Outline each uninfected red blood cell.
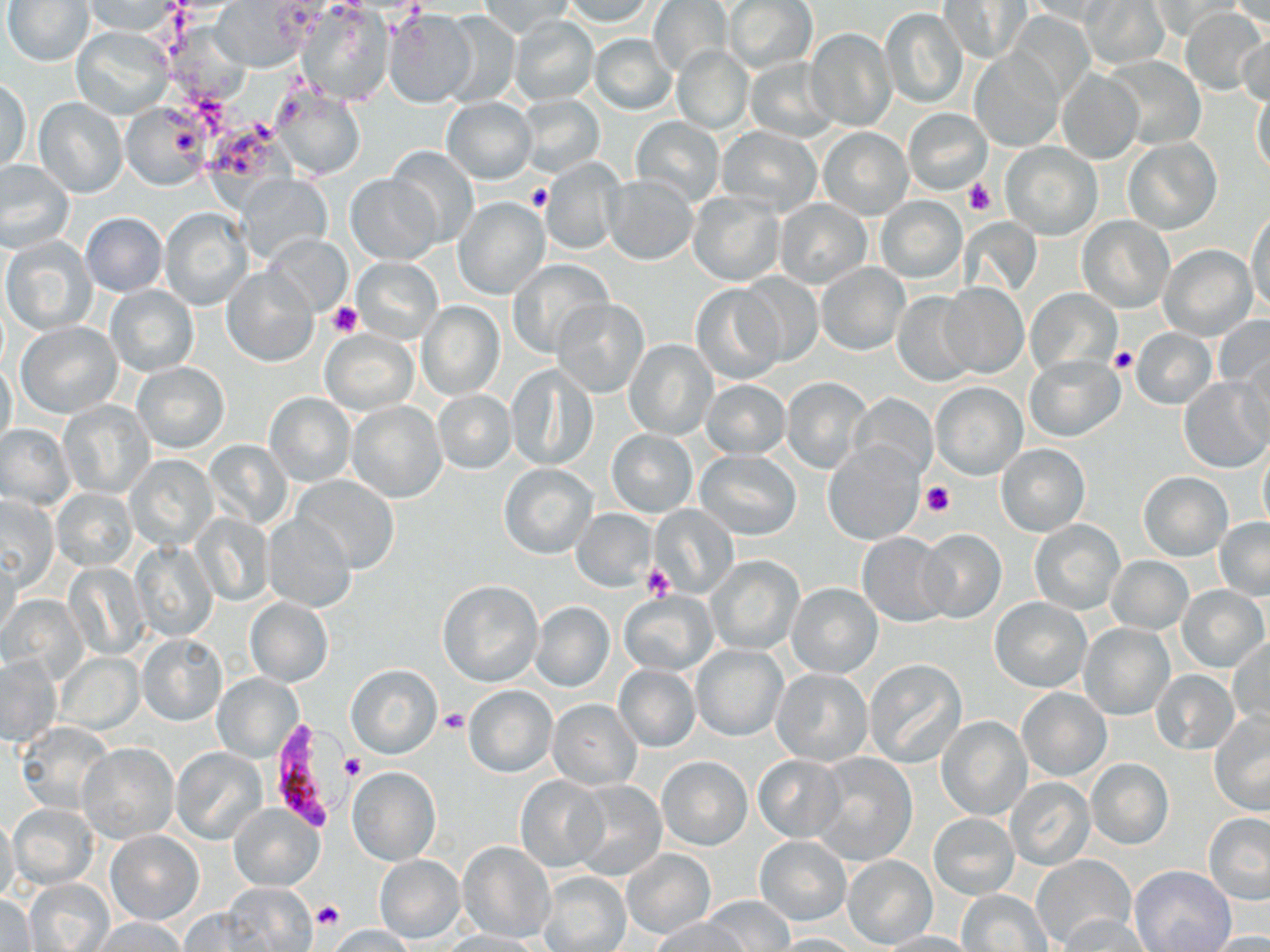

Approximate bounding boxes as named x1/y1/x2/y2 corners in pixels.
Uninfected red blood cells: (x1=4, y1=0, x2=94, y2=65), (x1=214, y1=0, x2=321, y2=70), (x1=559, y1=0, x2=662, y2=27), (x1=648, y1=0, x2=732, y2=76), (x1=725, y1=0, x2=816, y2=72), (x1=938, y1=0, x2=1029, y2=63), (x1=1084, y1=0, x2=1167, y2=68), (x1=1229, y1=0, x2=1269, y2=33), (x1=81, y1=1, x2=184, y2=38), (x1=477, y1=1, x2=575, y2=38), (x1=1020, y1=1, x2=1122, y2=25), (x1=1149, y1=1, x2=1242, y2=39), (x1=294, y1=5, x2=394, y2=106), (x1=880, y1=7, x2=970, y2=110), (x1=1182, y1=7, x2=1268, y2=96), (x1=382, y1=8, x2=478, y2=108), (x1=440, y1=12, x2=522, y2=107), (x1=507, y1=17, x2=599, y2=106), (x1=806, y1=26, x2=897, y2=133), (x1=71, y1=27, x2=173, y2=119), (x1=588, y1=33, x2=678, y2=116), (x1=1236, y1=35, x2=1269, y2=109), (x1=672, y1=45, x2=755, y2=135), (x1=969, y1=50, x2=1064, y2=152), (x1=1106, y1=55, x2=1206, y2=149), (x1=744, y1=57, x2=838, y2=142), (x1=1057, y1=68, x2=1142, y2=164), (x1=1, y1=77, x2=32, y2=171), (x1=1250, y1=84, x2=1269, y2=180), (x1=273, y1=86, x2=366, y2=182), (x1=515, y1=94, x2=605, y2=179), (x1=34, y1=97, x2=128, y2=198), (x1=441, y1=97, x2=536, y2=184), (x1=121, y1=105, x2=207, y2=189), (x1=904, y1=108, x2=991, y2=194), (x1=631, y1=117, x2=724, y2=206), (x1=716, y1=127, x2=823, y2=217), (x1=817, y1=127, x2=913, y2=219), (x1=1121, y1=137, x2=1221, y2=235), (x1=1001, y1=142, x2=1102, y2=240), (x1=385, y1=146, x2=481, y2=247), (x1=541, y1=156, x2=624, y2=257), (x1=0, y1=161, x2=75, y2=252), (x1=234, y1=173, x2=333, y2=266), (x1=345, y1=174, x2=440, y2=265), (x1=603, y1=175, x2=698, y2=265), (x1=687, y1=190, x2=785, y2=286), (x1=454, y1=195, x2=549, y2=300), (x1=875, y1=196, x2=966, y2=283), (x1=773, y1=197, x2=873, y2=289), (x1=160, y1=208, x2=253, y2=311), (x1=1247, y1=208, x2=1269, y2=316), (x1=79, y1=212, x2=168, y2=297), (x1=1076, y1=215, x2=1175, y2=313), (x1=263, y1=236, x2=351, y2=317), (x1=2, y1=237, x2=97, y2=334), (x1=1159, y1=244, x2=1256, y2=340), (x1=352, y1=257, x2=442, y2=343), (x1=508, y1=259, x2=611, y2=358), (x1=816, y1=263, x2=910, y2=356), (x1=222, y1=266, x2=318, y2=367), (x1=735, y1=273, x2=824, y2=368), (x1=937, y1=282, x2=1028, y2=379), (x1=690, y1=284, x2=784, y2=384), (x1=104, y1=285, x2=199, y2=377), (x1=1026, y1=289, x2=1121, y2=378), (x1=893, y1=291, x2=979, y2=386), (x1=553, y1=297, x2=651, y2=397), (x1=417, y1=300, x2=504, y2=400), (x1=1215, y1=314, x2=1270, y2=403), (x1=17, y1=322, x2=121, y2=418), (x1=321, y1=328, x2=418, y2=416), (x1=1131, y1=328, x2=1215, y2=409), (x1=624, y1=339, x2=719, y2=440), (x1=1025, y1=355, x2=1124, y2=442), (x1=0, y1=359, x2=18, y2=455), (x1=132, y1=362, x2=230, y2=454), (x1=506, y1=364, x2=595, y2=472), (x1=780, y1=377, x2=872, y2=474), (x1=1179, y1=377, x2=1270, y2=473), (x1=701, y1=379, x2=792, y2=459), (x1=930, y1=382, x2=1027, y2=481), (x1=433, y1=389, x2=516, y2=473), (x1=848, y1=392, x2=937, y2=481), (x1=265, y1=393, x2=355, y2=486), (x1=346, y1=401, x2=447, y2=503), (x1=59, y1=402, x2=154, y2=499), (x1=1, y1=425, x2=74, y2=509), (x1=607, y1=430, x2=697, y2=516), (x1=202, y1=440, x2=292, y2=529), (x1=824, y1=443, x2=923, y2=545), (x1=997, y1=443, x2=1090, y2=537), (x1=1258, y1=443, x2=1270, y2=537), (x1=695, y1=450, x2=800, y2=540), (x1=125, y1=454, x2=218, y2=551), (x1=499, y1=464, x2=599, y2=560), (x1=1138, y1=471, x2=1232, y2=561), (x1=291, y1=475, x2=400, y2=574), (x1=52, y1=487, x2=138, y2=570), (x1=0, y1=497, x2=59, y2=592), (x1=648, y1=505, x2=737, y2=598), (x1=572, y1=509, x2=656, y2=592), (x1=193, y1=513, x2=272, y2=606), (x1=261, y1=514, x2=357, y2=611), (x1=1027, y1=518, x2=1125, y2=616), (x1=1214, y1=518, x2=1270, y2=600), (x1=917, y1=528, x2=1006, y2=624), (x1=857, y1=532, x2=954, y2=627), (x1=130, y1=539, x2=216, y2=642), (x1=0, y1=553, x2=22, y2=640), (x1=706, y1=556, x2=805, y2=656), (x1=1106, y1=556, x2=1192, y2=633), (x1=65, y1=562, x2=148, y2=661), (x1=438, y1=581, x2=543, y2=686), (x1=788, y1=583, x2=881, y2=677), (x1=1177, y1=585, x2=1269, y2=673), (x1=618, y1=590, x2=718, y2=676), (x1=3, y1=595, x2=88, y2=682), (x1=245, y1=597, x2=333, y2=688), (x1=990, y1=597, x2=1091, y2=692), (x1=531, y1=601, x2=614, y2=692), (x1=1078, y1=622, x2=1175, y2=720), (x1=138, y1=632, x2=227, y2=726), (x1=1228, y1=637, x2=1269, y2=732), (x1=691, y1=645, x2=786, y2=740), (x1=56, y1=653, x2=143, y2=734), (x1=0, y1=657, x2=62, y2=745), (x1=864, y1=658, x2=967, y2=767), (x1=345, y1=664, x2=441, y2=758), (x1=614, y1=665, x2=700, y2=751), (x1=771, y1=668, x2=872, y2=766), (x1=1151, y1=670, x2=1239, y2=755), (x1=213, y1=674, x2=304, y2=762), (x1=464, y1=685, x2=557, y2=778), (x1=1016, y1=686, x2=1112, y2=781), (x1=548, y1=699, x2=642, y2=790), (x1=1210, y1=712, x2=1270, y2=815), (x1=937, y1=716, x2=1032, y2=820), (x1=17, y1=723, x2=115, y2=814), (x1=77, y1=743, x2=179, y2=842), (x1=170, y1=747, x2=268, y2=846), (x1=811, y1=754, x2=917, y2=865), (x1=657, y1=756, x2=752, y2=851), (x1=753, y1=756, x2=844, y2=841), (x1=1087, y1=758, x2=1174, y2=850), (x1=348, y1=767, x2=440, y2=865), (x1=515, y1=776, x2=607, y2=873), (x1=1005, y1=778, x2=1094, y2=870), (x1=572, y1=781, x2=668, y2=880), (x1=8, y1=802, x2=99, y2=889), (x1=229, y1=804, x2=322, y2=891), (x1=0, y1=812, x2=19, y2=907), (x1=1203, y1=813, x2=1270, y2=906), (x1=929, y1=814, x2=1019, y2=898), (x1=105, y1=831, x2=203, y2=926), (x1=756, y1=835, x2=850, y2=925), (x1=458, y1=841, x2=556, y2=943), (x1=621, y1=848, x2=716, y2=938), (x1=1032, y1=854, x2=1134, y2=950), (x1=374, y1=855, x2=465, y2=944), (x1=843, y1=855, x2=938, y2=948), (x1=1130, y1=865, x2=1235, y2=952), (x1=536, y1=870, x2=631, y2=952), (x1=24, y1=879, x2=114, y2=952), (x1=220, y1=885, x2=318, y2=951), (x1=957, y1=890, x2=1052, y2=952), (x1=0, y1=892, x2=37, y2=950), (x1=703, y1=896, x2=794, y2=952), (x1=179, y1=907, x2=274, y2=949), (x1=652, y1=915, x2=746, y2=952), (x1=1055, y1=915, x2=1151, y2=952), (x1=88, y1=917, x2=191, y2=951), (x1=324, y1=925, x2=420, y2=951), (x1=437, y1=930, x2=543, y2=951), (x1=876, y1=931, x2=976, y2=952), (x1=1200, y1=932, x2=1270, y2=951), (x1=771, y1=933, x2=863, y2=952).

Summary:
  - Platelet locations: (x1=963, y1=178, x2=998, y2=216), (x1=527, y1=184, x2=551, y2=211), (x1=327, y1=300, x2=363, y2=337), (x1=1109, y1=346, x2=1135, y2=374), (x1=921, y1=480, x2=957, y2=517), (x1=645, y1=566, x2=675, y2=601), (x1=440, y1=709, x2=470, y2=733), (x1=341, y1=754, x2=367, y2=780), (x1=312, y1=900, x2=345, y2=930)
  - Plasmodium falciparum-infected red blood cell locations: (x1=268, y1=718, x2=358, y2=830)
  - Slide-level diagnosis: Plasmodium falciparum
  - Preparation: thin blood smear
  - Magnification: 1000x
  - Image size: 1270×952 pixels
  - Modality: optical microscopy
  - Stain: May-Grünwald-Giemsa
  - Field of view: one of a larger specimen